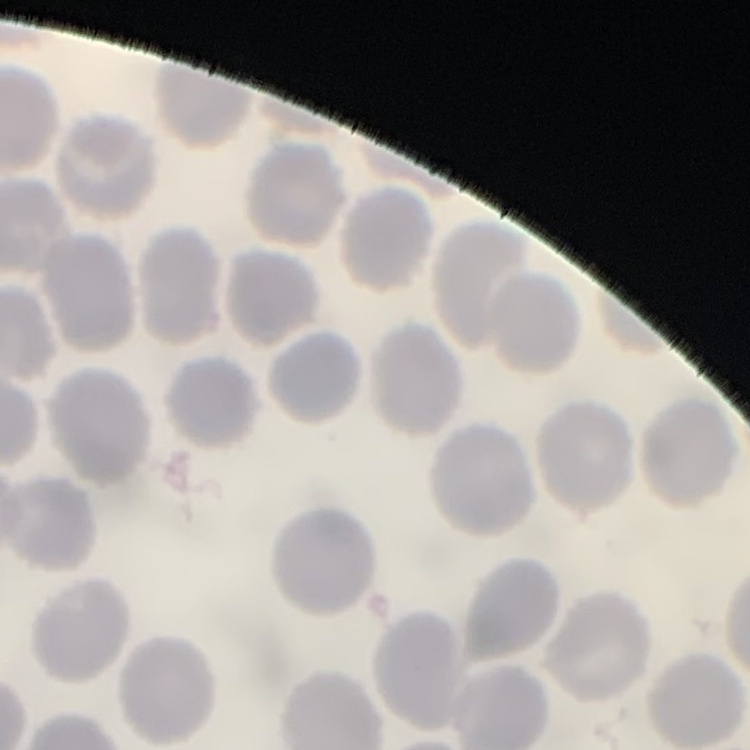
Summary:
  - Red blood cell morphology: no rouleaux formation
  - Preparation: thin peripheral smear
  - Image type: square crop of a larger photomicrograph
  - Stain: Field's or Giemsa